Comment on the morphology of the red blood cells.
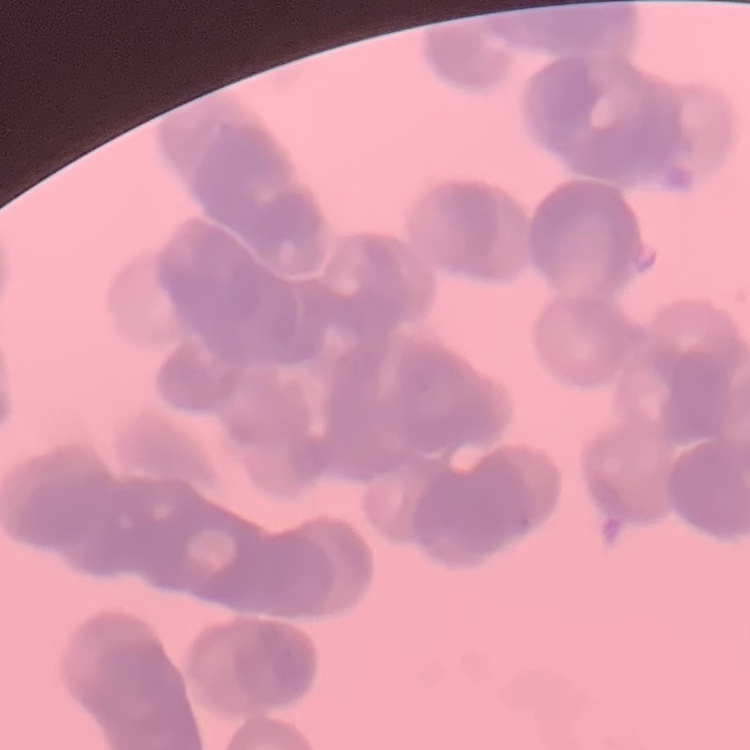
They show rouleaux formation.

Summary:
  - Preparation: thin blood smear
  - Stain: Field's or Giemsa
  - Image type: one tile cut from a larger photomicrograph